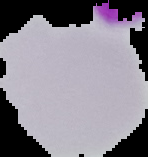

Summary:
  - Image type: segmented cell region on a black background
  - Preparation: thin blood smear
  - Image size: 148×157 pixels
  - Malaria status: uninfected